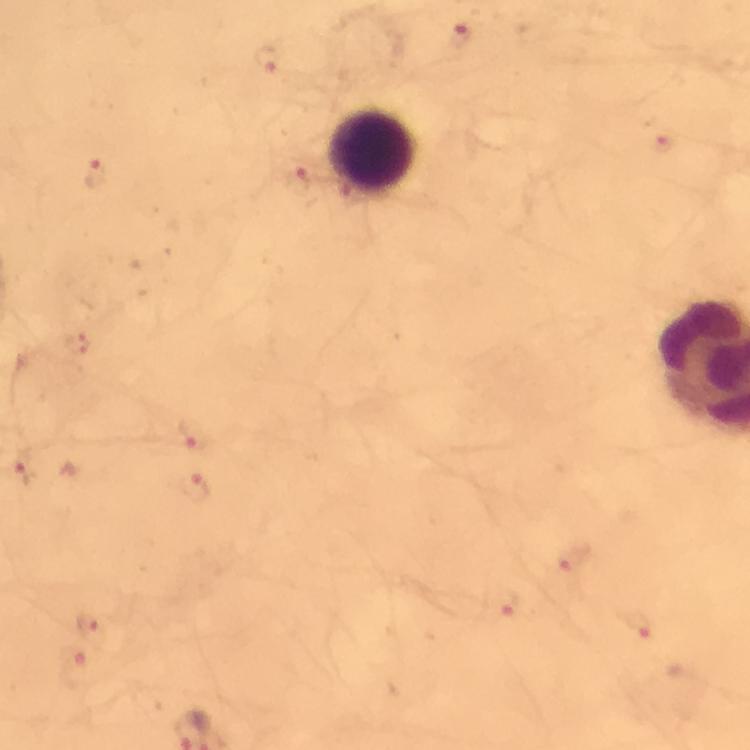
Approximate centers as (x, y) in pixels. Malaria parasite locations: (461, 35), (267, 58), (664, 145), (99, 174), (305, 174), (76, 343), (195, 433), (24, 465), (194, 489), (575, 561), (507, 608), (640, 624), (93, 626), (78, 670). Giemsa stain. Image is 750×750 pixels. Cropped region of a single field of view. Immersion oil was used. At 100x magnification. Thick smear. From a diagnostic examination for malaria. Photographed through the microscope with a smartphone camera.